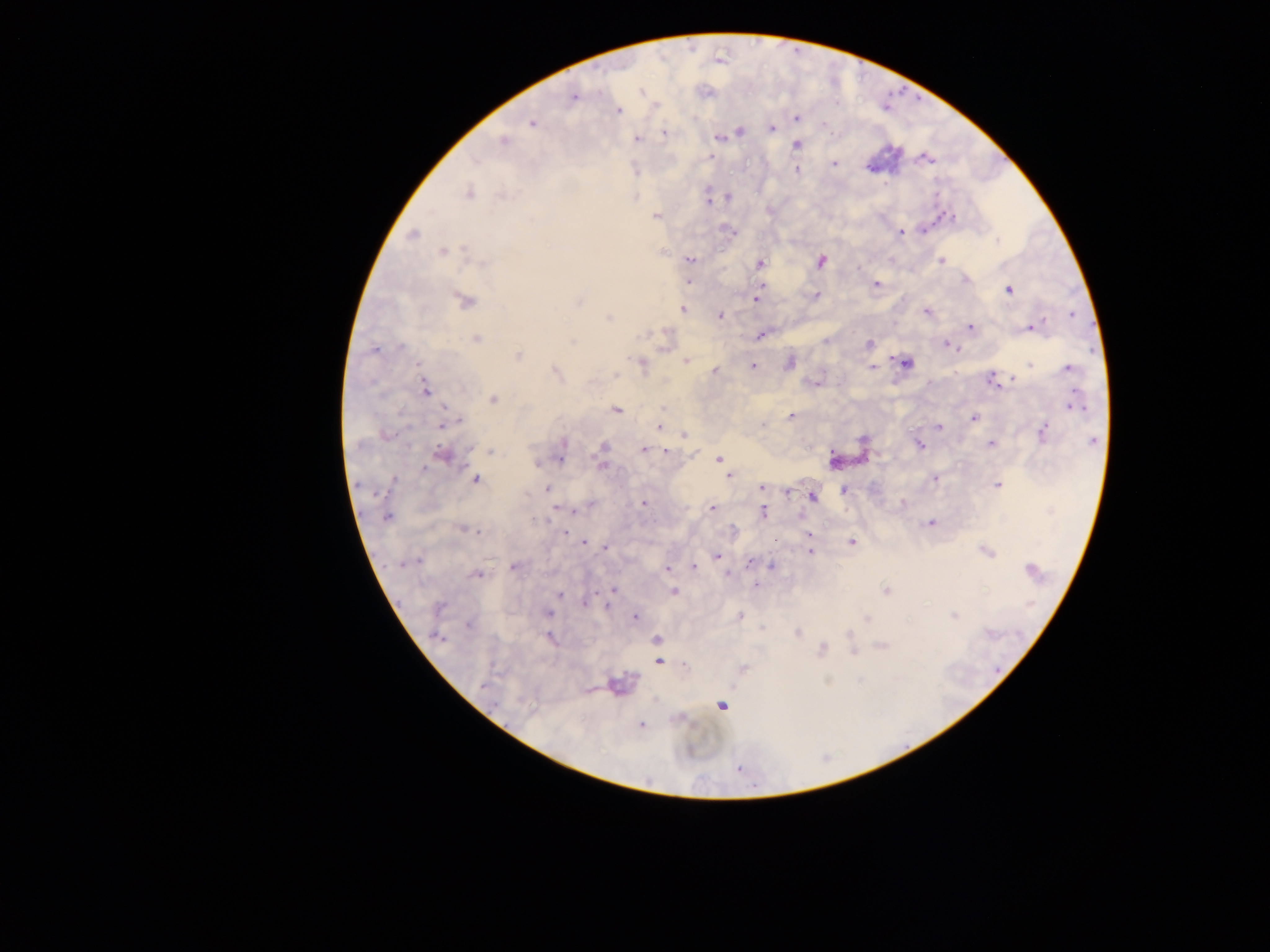
Approximate centers as (x, y) in pixels.
Summary:
  - Malaria parasite locations: (574, 98), (618, 110), (796, 118), (532, 123), (771, 128), (740, 131), (664, 132), (719, 137), (636, 139), (502, 141), (795, 144), (709, 156), (925, 158), (834, 162), (796, 170), (468, 193), (728, 197), (708, 201), (655, 215), (944, 216), (731, 232), (900, 232), (412, 234), (444, 251), (689, 259), (941, 260), (820, 261), (758, 264), (964, 278), (688, 281), (875, 284), (1008, 289), (814, 295), (755, 298), (464, 300), (682, 310), (926, 311), (719, 316), (608, 317), (970, 327), (1030, 327), (761, 334), (476, 339), (868, 344), (948, 346), (374, 350), (518, 356), (685, 360), (789, 362), (904, 362), (641, 363), (753, 366), (872, 368), (1068, 368), (714, 370), (555, 373), (992, 379), (816, 383), (424, 391), (493, 399), (1074, 406), (615, 409), (791, 416), (973, 418), (443, 422), (763, 424), (659, 425), (938, 426), (1043, 432), (684, 434), (919, 443), (990, 443), (645, 449), (665, 450), (490, 451), (441, 455), (560, 455), (719, 459), (536, 462), (601, 463), (728, 475), (475, 479), (934, 479), (996, 485), (761, 487), (547, 489), (844, 490), (787, 491), (811, 496), (642, 502), (902, 503), (711, 508), (574, 509), (763, 512), (387, 517), (930, 523), (462, 529), (565, 532), (808, 535), (852, 542), (584, 543), (605, 547), (984, 550), (809, 552), (717, 556), (408, 562), (749, 562), (512, 566), (692, 566), (771, 566), (666, 567), (727, 574), (477, 575), (756, 583), (613, 590), (885, 590), (673, 591), (559, 594), (584, 602), (607, 604), (438, 607), (548, 613), (954, 615), (635, 616), (740, 616), (867, 618), (469, 624), (796, 632), (437, 636), (549, 638), (656, 640), (881, 646), (820, 650), (852, 652), (658, 660), (683, 666), (742, 668), (617, 685), (721, 706), (640, 724)
  - Preparation: thick blood smear
  - Field of view: single
  - Capture: mobile-phone photograph through a microscope
  - Image size: 1270×952 pixels
  - Country: Ghana